Report the malaria status of this cell.
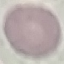

Uninfected.

capture = smartphone camera at the microscope eyepiece
image type = cell patch, automatically extracted from a larger field of view and resized to 64 × 64 pixels
preparation = thin blood smear
stain = Giemsa